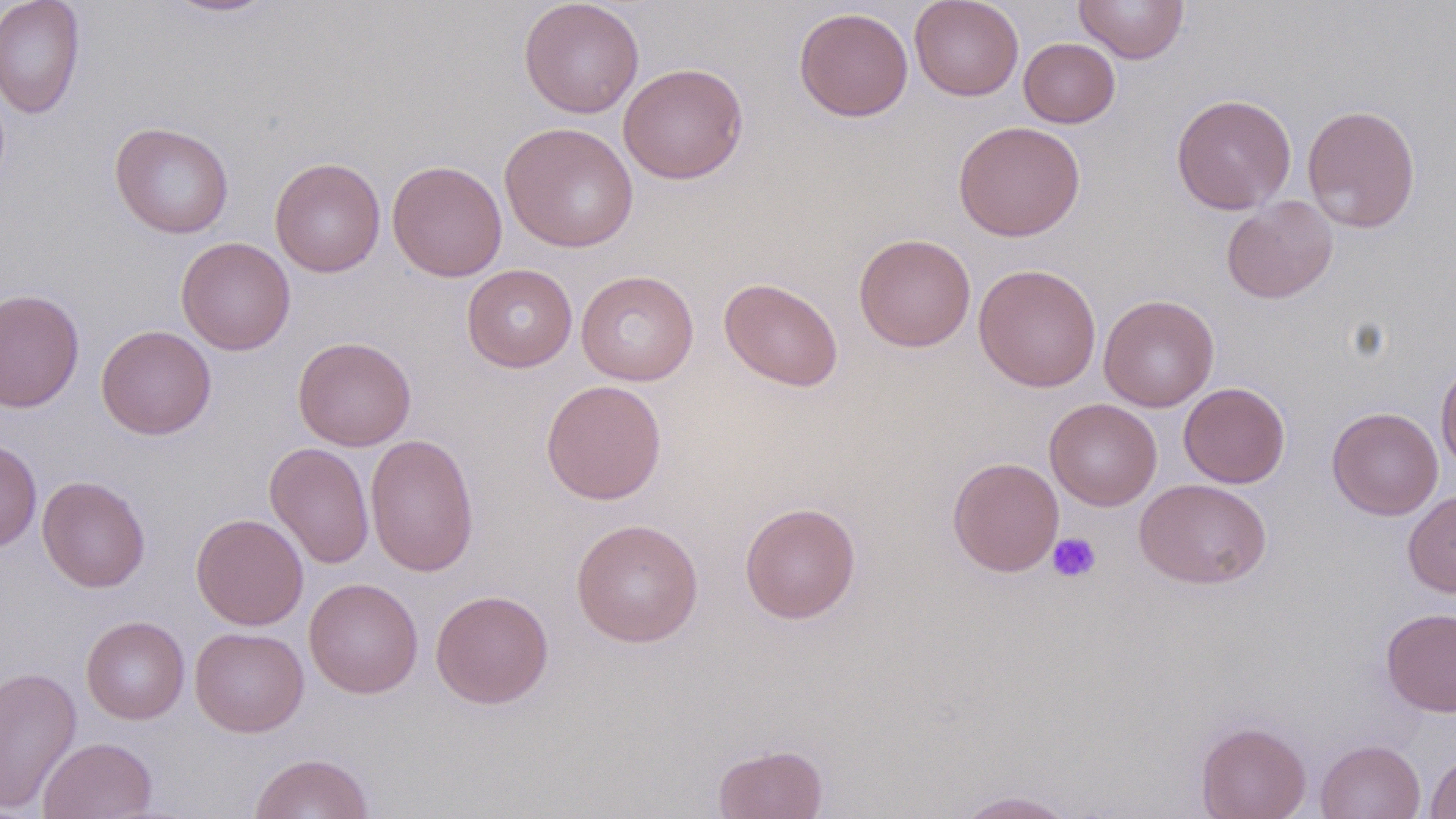
Summary:
  - Coordinate format: approximate bounding boxes as (x1, y1, x2, y2) in pixels
  - Uninfected red blood cell locations: (0, 0, 86, 119), (160, 0, 281, 18), (519, 0, 644, 118), (909, 0, 1024, 101), (1073, 0, 1190, 64), (794, 7, 913, 122), (1018, 37, 1120, 128), (618, 62, 748, 184), (1170, 93, 1297, 215), (1301, 104, 1421, 233), (109, 121, 234, 239), (500, 121, 639, 252), (953, 121, 1085, 241), (269, 157, 386, 277), (387, 159, 507, 281), (1221, 196, 1338, 304), (854, 233, 976, 352), (176, 236, 296, 354), (973, 263, 1101, 392), (462, 264, 577, 372), (575, 270, 699, 386), (720, 278, 843, 392), (0, 288, 85, 413), (1099, 295, 1219, 412), (96, 324, 217, 440), (293, 336, 416, 451), (1436, 359, 1456, 473), (540, 379, 667, 505), (1178, 382, 1290, 488), (1045, 398, 1162, 511), (1327, 407, 1443, 520), (365, 433, 479, 577), (0, 439, 42, 552), (264, 442, 375, 569), (948, 457, 1064, 576), (37, 475, 151, 592), (1134, 478, 1272, 589), (1403, 489, 1456, 597), (739, 501, 861, 624), (191, 514, 309, 630), (571, 518, 704, 647), (303, 577, 423, 698), (430, 589, 554, 709), (1380, 608, 1456, 717), (81, 615, 190, 724), (190, 626, 309, 737), (0, 666, 82, 813), (1195, 720, 1312, 818), (39, 736, 158, 819), (1315, 739, 1426, 819), (713, 743, 828, 819), (249, 752, 375, 818), (1424, 752, 1456, 818), (954, 789, 1079, 818)
  - Platelet locations: (1046, 532, 1101, 583)
  - Slide-level diagnosis: negative for blood parasites
  - Preparation: thin blood smear
  - Image size: 1456×819 pixels
  - Modality: light microscopy
  - Stain: May-Grünwald-Giemsa
  - Magnification: 1000x
  - Field of view: one of a larger specimen